Evaluate for malaria.
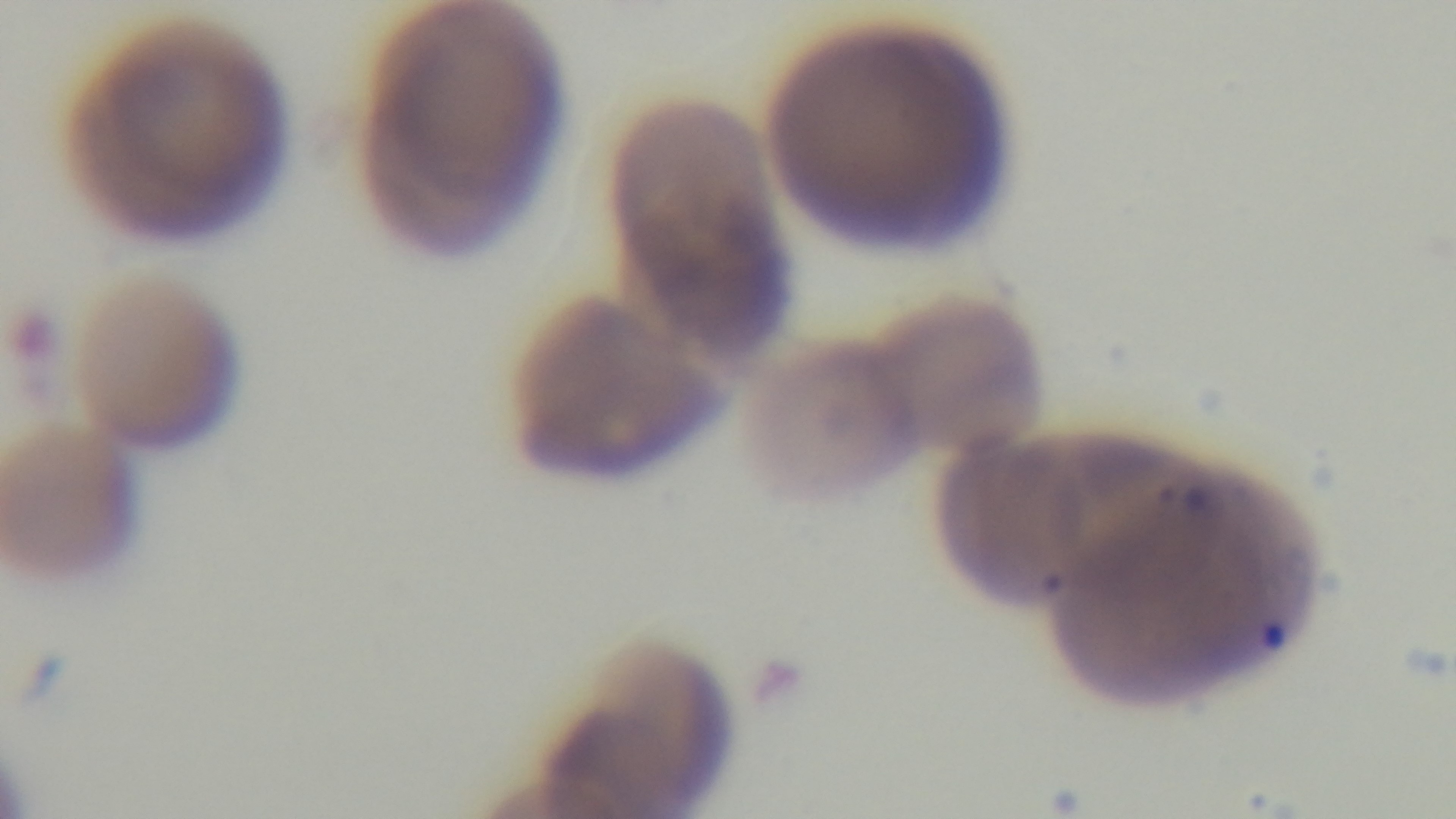

Infected.

preparation = thin smear
field of view = one from the slide
objective = 100x oil immersion
modality = light microscopy
capture = mounted 4K digital camera
stain = Giemsa